Locate every Plasmodium malariae-infected red blood cell.
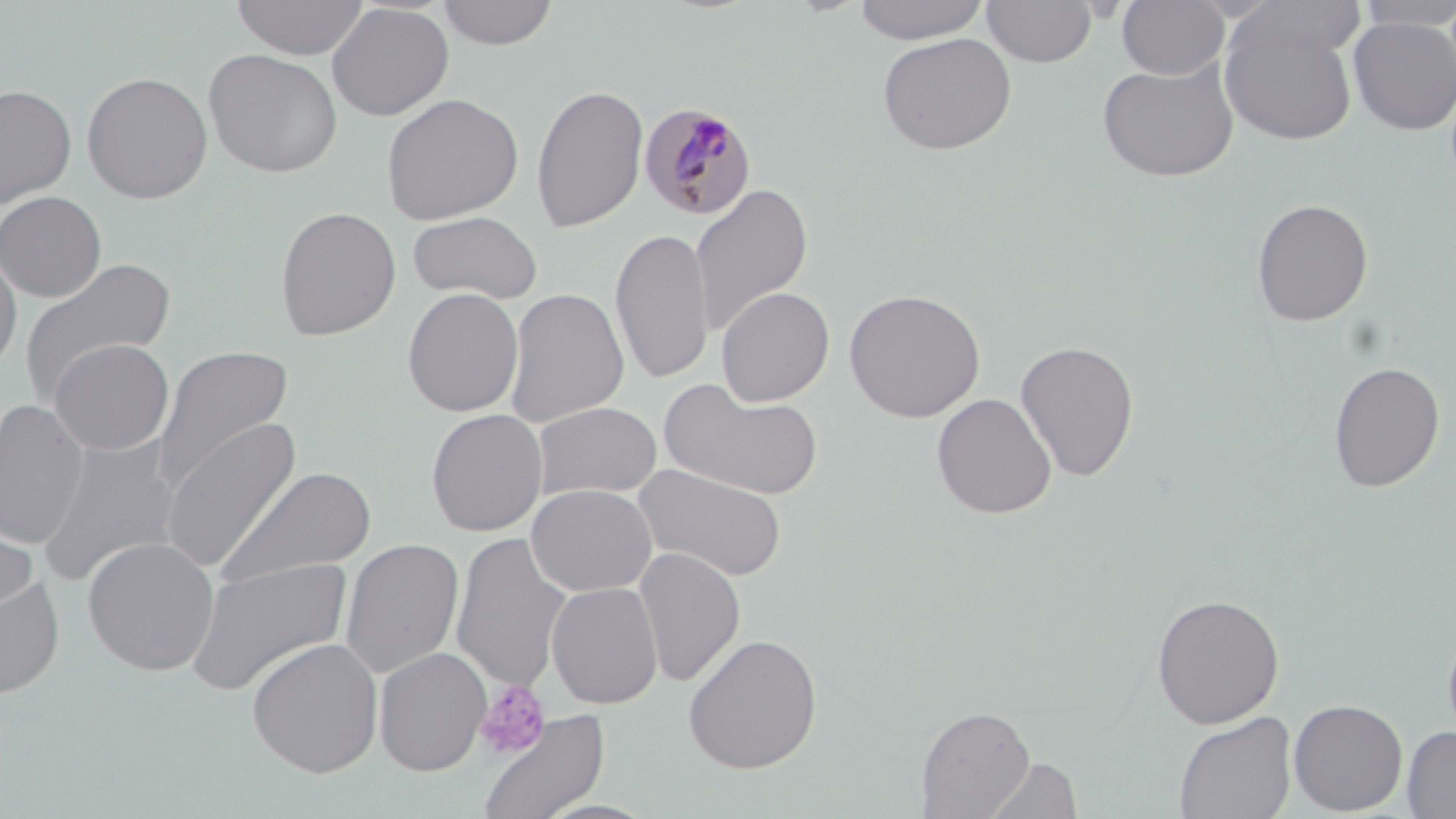

Approximate bounding boxes as (x1,y1)-(x2,y2) corner pairs in pixels.
Plasmodium malariae-infected red blood cells: (639,103)-(758,220).

Platelet locations: (474,679)-(552,760). Uninfected red blood cell locations: (231,0)-(369,60), (437,0)-(560,50), (853,0)-(990,44), (1115,0)-(1230,81), (1229,0)-(1368,65), (981,1)-(1097,68), (1352,1)-(1456,31), (327,3)-(454,121), (1218,14)-(1357,147), (1347,16)-(1456,135), (876,32)-(1017,155), (203,49)-(343,178), (1097,60)-(1239,182), (81,71)-(213,204), (531,83)-(648,233), (0,84)-(77,208), (380,92)-(524,225), (690,182)-(813,338), (0,191)-(107,302), (1251,198)-(1374,327), (274,206)-(402,341), (407,211)-(543,305), (611,227)-(714,386), (0,244)-(22,381), (18,256)-(176,407), (716,286)-(834,407), (504,287)-(629,428), (402,288)-(524,417), (844,288)-(985,422), (48,339)-(174,456), (1015,339)-(1140,482), (153,345)-(294,492), (1327,361)-(1446,492), (659,379)-(822,501), (932,393)-(1056,519), (0,398)-(90,550), (532,402)-(662,501), (426,408)-(548,536), (160,416)-(303,573), (37,436)-(183,588), (632,462)-(788,582), (213,466)-(377,590), (526,483)-(656,596), (0,506)-(40,625), (451,532)-(573,692), (82,536)-(220,676), (340,538)-(464,679), (633,547)-(746,686), (184,556)-(353,698), (0,575)-(65,700), (546,581)-(663,709), (1150,593)-(1285,729), (1441,622)-(1456,748), (682,633)-(823,774), (246,637)-(384,778), (373,647)-(491,776), (1288,698)-(1407,815), (915,704)-(1035,818), (474,709)-(610,819), (1173,711)-(1297,819), (1402,725)-(1456,818), (982,755)-(1084,818). Slide-level diagnosis: Plasmodium malariae. Thin blood film. One field of a larger specimen. 1000x magnification. Image is 1456×819 pixels. Optical microscopy. May-Grünwald-Giemsa stain.